Report the malaria status of this cell.
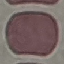

Uninfected.

Summary:
  - Stain: Giemsa
  - Image type: cell patch, automatically extracted from a larger field of view and resized to 64 × 64 pixels
  - Preparation: thin smear
  - Capture: smartphone camera at the microscope eyepiece